Outline each white blood cell.
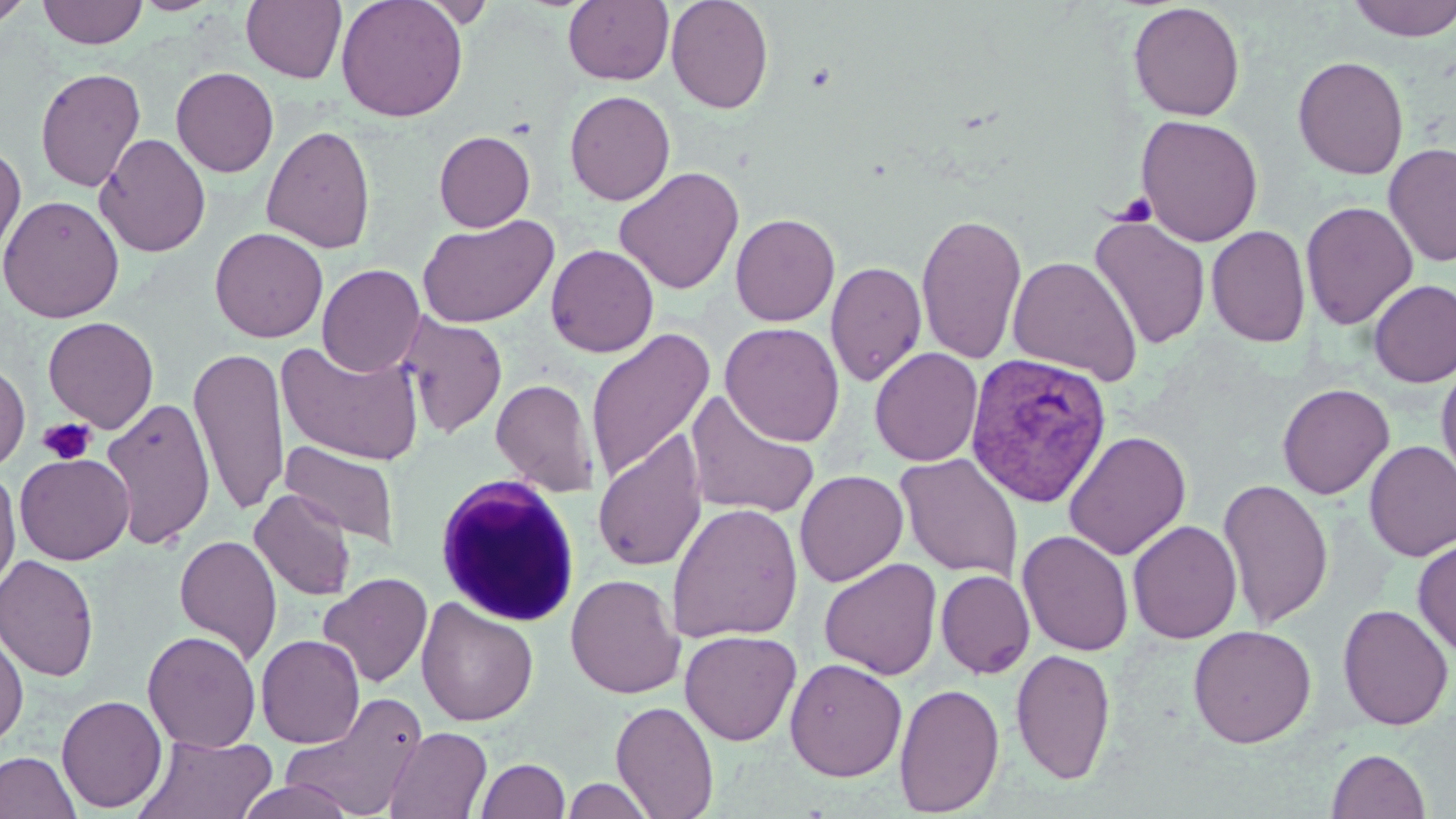
Approximate bounding boxes as named x1/y1/x2/y2 corners in pixels.
White blood cells: (x1=432, y1=475, x2=582, y2=627).

Summary:
  - Plasmodium vivax-infected red blood cell locations: (x1=964, y1=352, x2=1113, y2=509)
  - Uninfected red blood cell locations: (x1=0, y1=0, x2=34, y2=28), (x1=38, y1=0, x2=147, y2=48), (x1=132, y1=0, x2=223, y2=15), (x1=241, y1=0, x2=347, y2=84), (x1=335, y1=0, x2=468, y2=122), (x1=411, y1=0, x2=499, y2=27), (x1=563, y1=0, x2=673, y2=85), (x1=666, y1=0, x2=774, y2=114), (x1=1346, y1=0, x2=1456, y2=42), (x1=1128, y1=2, x2=1245, y2=121), (x1=1293, y1=56, x2=1409, y2=179), (x1=171, y1=66, x2=279, y2=177), (x1=35, y1=67, x2=146, y2=192), (x1=564, y1=90, x2=675, y2=206), (x1=1136, y1=114, x2=1263, y2=246), (x1=262, y1=125, x2=376, y2=253), (x1=434, y1=131, x2=535, y2=232), (x1=95, y1=133, x2=211, y2=257), (x1=0, y1=140, x2=26, y2=266), (x1=1383, y1=142, x2=1456, y2=267), (x1=614, y1=166, x2=744, y2=295), (x1=0, y1=195, x2=124, y2=323), (x1=1300, y1=201, x2=1418, y2=330), (x1=916, y1=212, x2=1026, y2=365), (x1=730, y1=213, x2=840, y2=326), (x1=417, y1=215, x2=558, y2=328), (x1=1090, y1=215, x2=1210, y2=349), (x1=1206, y1=225, x2=1311, y2=347), (x1=209, y1=227, x2=328, y2=342), (x1=546, y1=244, x2=659, y2=357), (x1=1008, y1=256, x2=1142, y2=384), (x1=825, y1=261, x2=927, y2=386), (x1=317, y1=264, x2=425, y2=376), (x1=1369, y1=279, x2=1456, y2=388), (x1=399, y1=313, x2=507, y2=438), (x1=43, y1=316, x2=159, y2=433), (x1=720, y1=322, x2=844, y2=447), (x1=585, y1=327, x2=714, y2=486), (x1=275, y1=340, x2=424, y2=466), (x1=189, y1=347, x2=290, y2=517), (x1=869, y1=347, x2=984, y2=467), (x1=1436, y1=356, x2=1456, y2=489), (x1=0, y1=360, x2=30, y2=471), (x1=491, y1=378, x2=599, y2=496), (x1=1277, y1=383, x2=1394, y2=499), (x1=684, y1=390, x2=821, y2=521), (x1=100, y1=396, x2=215, y2=550), (x1=592, y1=430, x2=708, y2=572), (x1=1064, y1=430, x2=1191, y2=561), (x1=280, y1=441, x2=401, y2=548), (x1=1364, y1=441, x2=1456, y2=561), (x1=14, y1=452, x2=134, y2=565), (x1=895, y1=453, x2=1024, y2=581), (x1=0, y1=466, x2=21, y2=595), (x1=794, y1=470, x2=908, y2=587), (x1=1217, y1=476, x2=1333, y2=630), (x1=249, y1=488, x2=356, y2=601), (x1=667, y1=502, x2=803, y2=643), (x1=1127, y1=519, x2=1242, y2=644), (x1=1017, y1=530, x2=1134, y2=656), (x1=174, y1=534, x2=282, y2=664), (x1=1413, y1=538, x2=1456, y2=658), (x1=0, y1=554, x2=100, y2=682), (x1=818, y1=558, x2=942, y2=680), (x1=936, y1=570, x2=1035, y2=678), (x1=317, y1=572, x2=433, y2=688), (x1=565, y1=573, x2=684, y2=698), (x1=416, y1=598, x2=538, y2=726), (x1=1337, y1=603, x2=1454, y2=731), (x1=1187, y1=624, x2=1317, y2=748), (x1=0, y1=627, x2=29, y2=747), (x1=680, y1=629, x2=802, y2=745), (x1=143, y1=630, x2=261, y2=753), (x1=256, y1=634, x2=365, y2=748), (x1=1010, y1=648, x2=1116, y2=785), (x1=785, y1=658, x2=907, y2=781), (x1=894, y1=682, x2=1005, y2=816), (x1=282, y1=692, x2=429, y2=817), (x1=56, y1=694, x2=167, y2=813), (x1=610, y1=699, x2=719, y2=818), (x1=384, y1=726, x2=493, y2=819), (x1=135, y1=733, x2=278, y2=818), (x1=1326, y1=748, x2=1431, y2=819), (x1=0, y1=751, x2=81, y2=819), (x1=475, y1=758, x2=570, y2=819), (x1=562, y1=777, x2=655, y2=819), (x1=234, y1=778, x2=358, y2=819)
  - Platelet locations: (x1=1113, y1=191, x2=1158, y2=228), (x1=38, y1=418, x2=95, y2=466)
  - Slide-level diagnosis: Plasmodium vivax
  - Stain: May-Grünwald-Giemsa
  - Magnification: 1000x
  - Modality: optical microscopy
  - Field of view: one of a larger specimen
  - Image size: 1456×819 pixels
  - Preparation: thin blood film